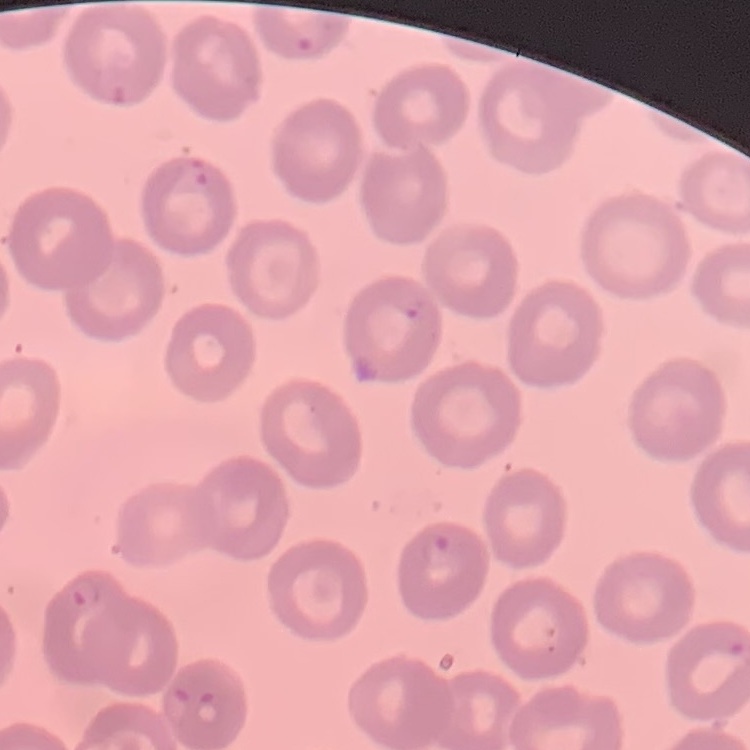

The erythrocytes show no rouleaux formation. Thin blood smear. Stained with either Field's or Giemsa. One tile cut from a larger photomicrograph.